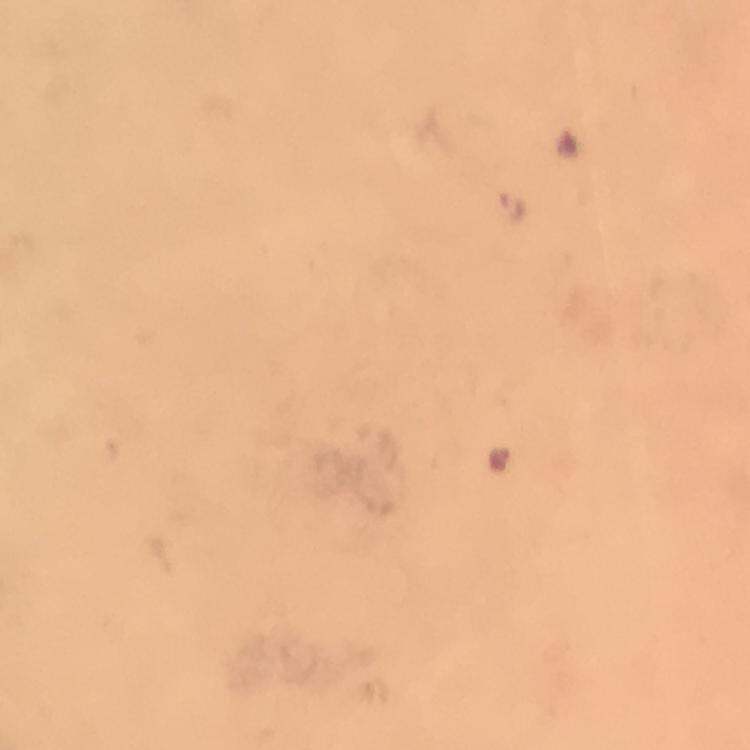

Approximate centers as [x, y] in pixels. Plasmodium parasite locations: [514, 205], [498, 457]. From a diagnostic examination for malaria. Photographed with a smartphone mounted on the microscope. Giemsa-stained preparation. 100x magnification. Immersion oil was used. Image is 750×750 pixels. Thick smear. A crop from one field of view.